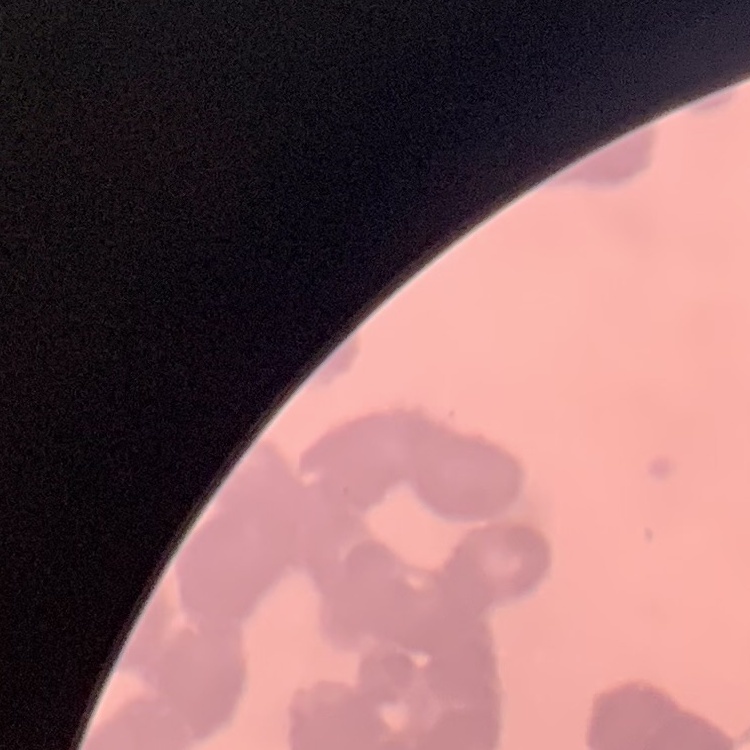

Summary:
  - Red blood cell morphology: rouleaux formation
  - Stain: Field's or Giemsa
  - Preparation: thin blood smear
  - Image type: square crop of a larger photomicrograph